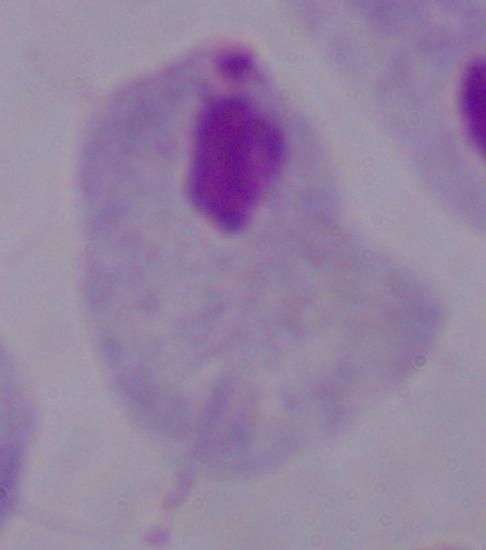
Summary:
  - Magnification: 1000x
  - Modality: micrograph
  - Identification: trichomonad